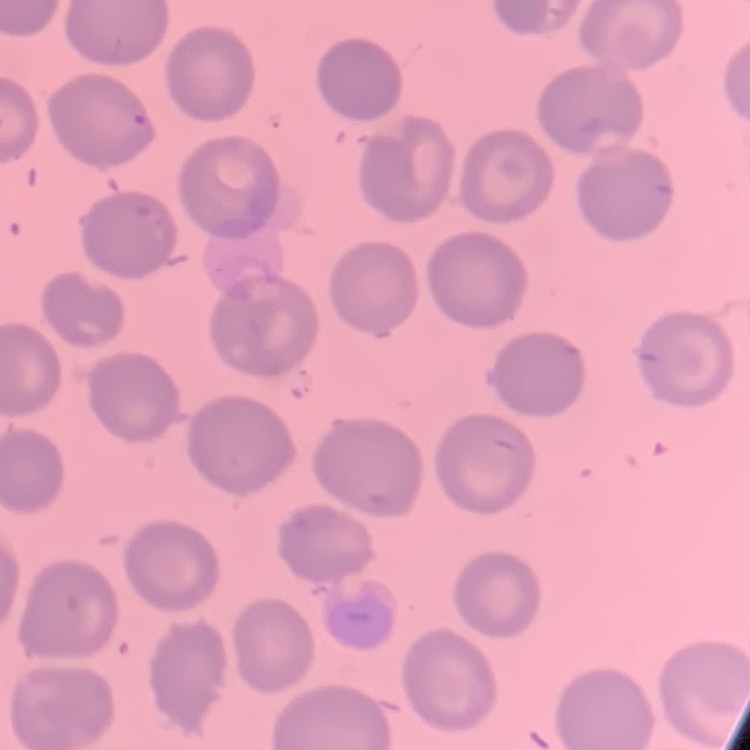
The erythrocytes show no rouleaux formation. Square crop of a larger photomicrograph. Thin peripheral smear. Stained with either Field's or Giemsa.